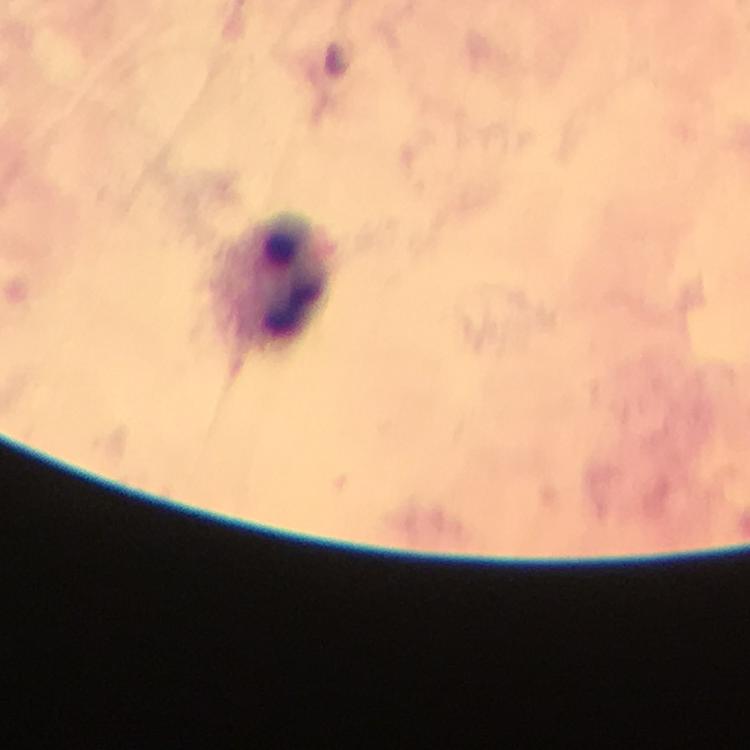

Approximate centers as {x, y} in pixels.
Summary:
  - Leukocyte locations: {279, 281}
  - Plasmodium parasites: none detected
  - Image size: 750×750 pixels
  - Preparation: thick smear
  - Immersion oil: used
  - Context: from a malaria diagnostic workup
  - Magnification: 100x
  - Stain: Giemsa
  - Cropped from: a single field of view
  - Capture: smartphone mounted on the microscope